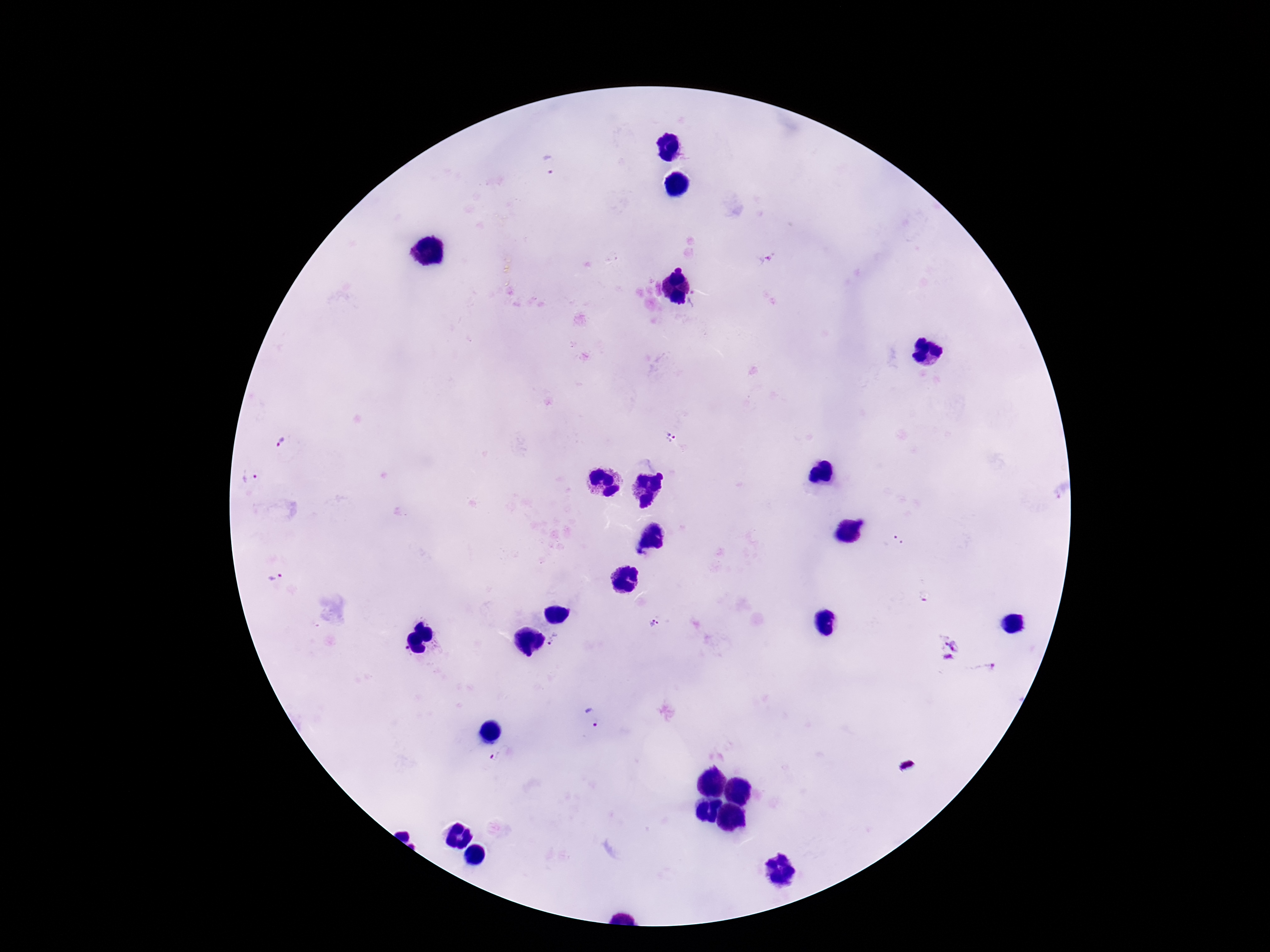
magnification = 100x
patient malaria status = infected
preparation = thick blood film
field of view = one from this slide
image size = 1270×952 pixels
stain = Giemsa
Plasmodium parasite locations = approximate centers as (x, y) in pixels: (551, 166), (670, 438), (282, 441), (251, 478), (275, 577), (658, 623), (556, 641), (951, 651), (985, 670), (592, 718), (499, 756)
capture = smartphone camera through the microscope eyepiece